State which parasite is depicted.
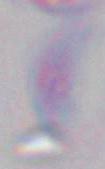
Toxoplasma gondii.

magnification = 1000x
modality = micrograph